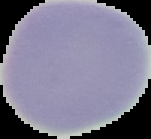
Image is 151×139 pixels. Segmented cell region on a black background. Malaria status: uninfected. From a thin blood film.